Classify this cell by malaria status.
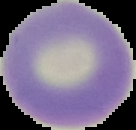

Uninfected.

Summary:
  - Preparation: thin blood film
  - Image type: segmented cell region on a black background
  - Image size: 136×130 pixels